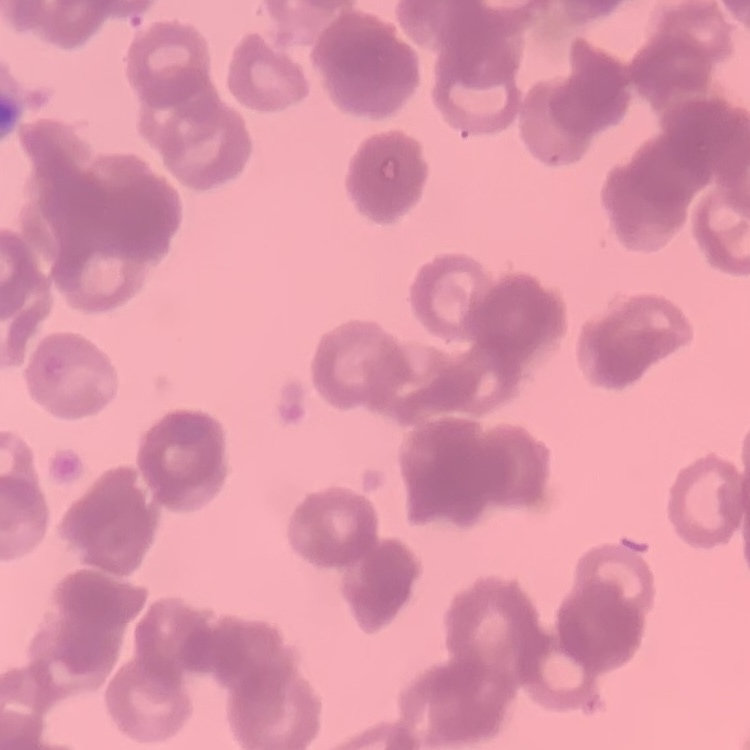
red blood cell morphology = rouleaux formation
preparation = thin peripheral smear
image type = one tile cut from a larger photomicrograph
stain = Field's or Giemsa